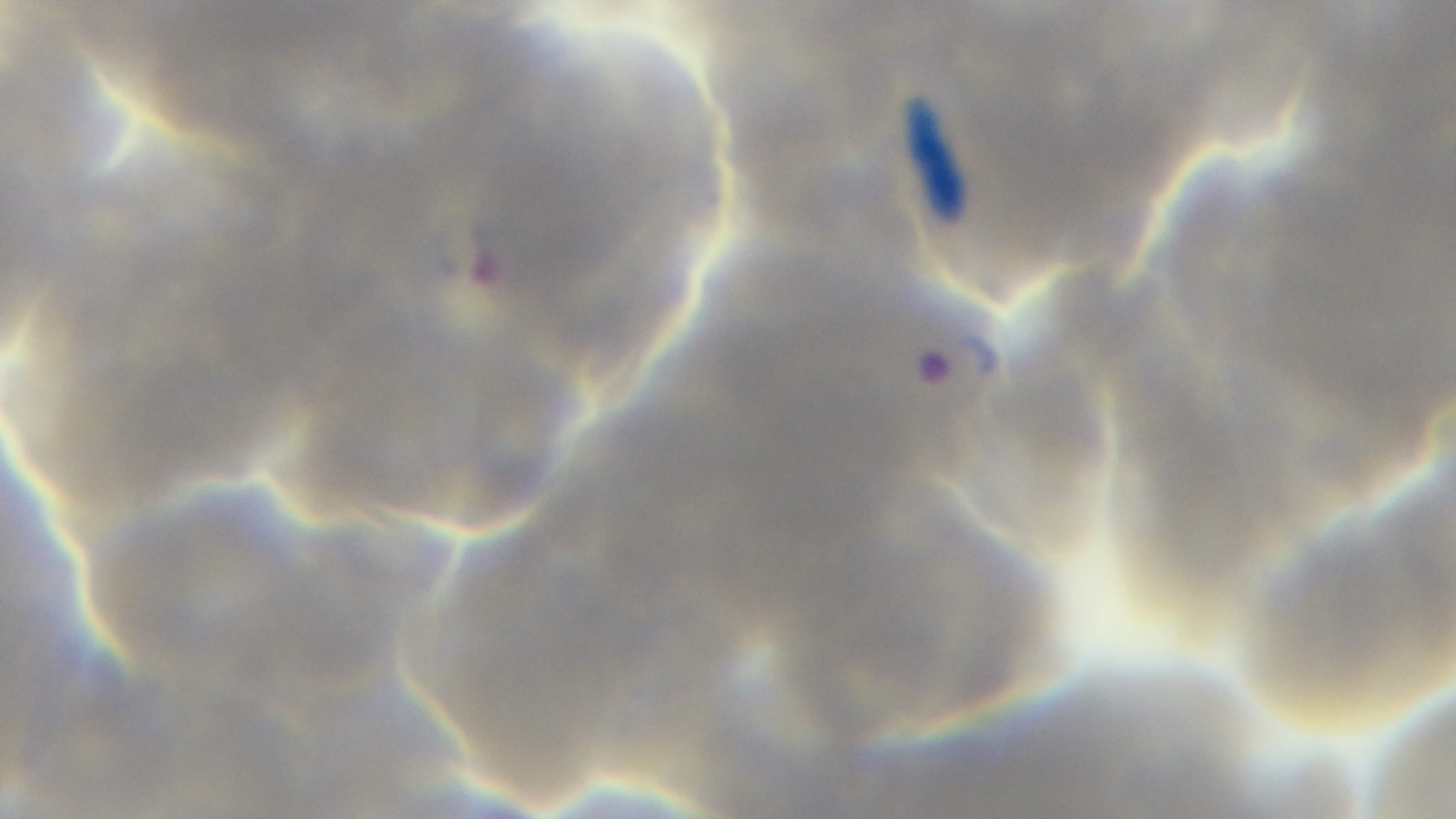

stain: Giemsa
modality: light microscopy
preparation: thin smear
capture: mounted 4K digital camera
field_of_view: single
malaria_status: infected
objective: 100x oil immersion